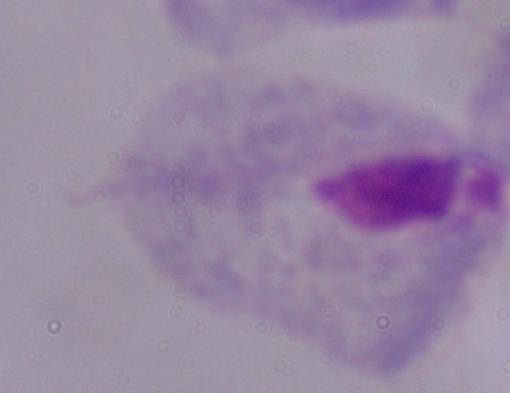

Summary:
  - Magnification: 1000x
  - Modality: photomicrograph
  - Identification: trichomonad